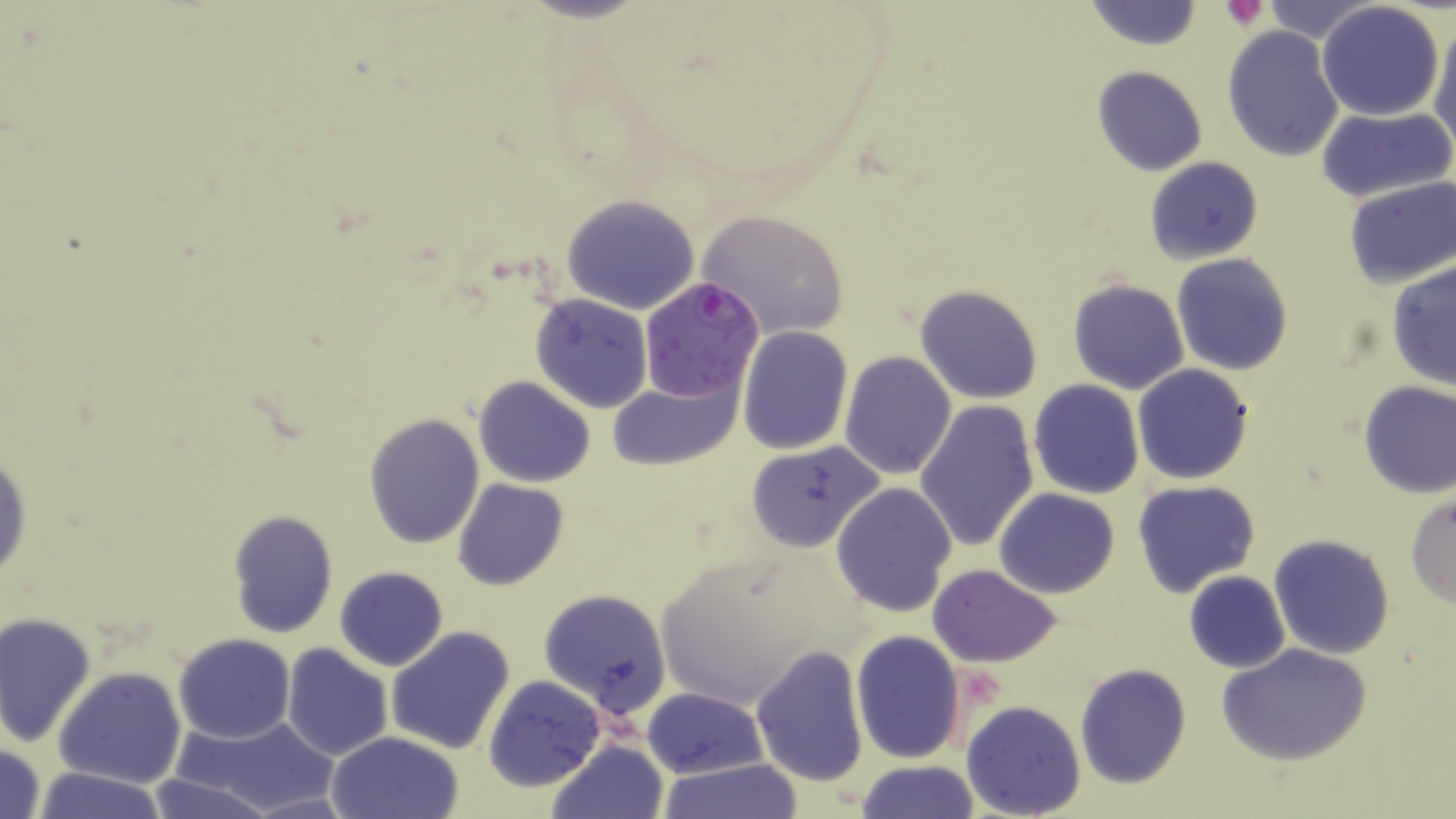
Approximate bounding boxes as (x1,y1)-(x2,y2) corner pairs in pixels. Plasmodium falciparum-infected red blood cell locations: (637,277)-(763,403). Platelet locations: (1222,1)-(1271,31). Uninfected red blood cell locations: (1085,0)-(1202,52), (1256,0)-(1383,45), (1315,2)-(1445,122), (1430,12)-(1456,149), (1222,27)-(1341,158), (1091,65)-(1207,176), (1316,105)-(1455,204), (1143,156)-(1262,265), (1343,178)-(1456,288), (561,195)-(701,314), (696,208)-(849,339), (1172,253)-(1293,374), (1387,262)-(1456,391), (1066,278)-(1190,394), (915,285)-(1042,403), (531,292)-(652,411), (737,325)-(852,453), (839,351)-(956,479), (1132,364)-(1254,484), (474,376)-(595,488), (608,376)-(741,472), (1029,378)-(1144,499), (1357,379)-(1456,497), (915,400)-(1038,551), (363,412)-(485,548), (0,441)-(32,589), (744,442)-(886,552), (451,478)-(570,591), (1131,481)-(1261,599), (832,483)-(958,616), (995,488)-(1119,598), (1406,494)-(1456,606), (226,509)-(339,640), (1268,534)-(1395,659), (650,550)-(842,707), (927,564)-(1061,667), (335,565)-(447,672), (1183,571)-(1290,673), (538,588)-(671,718), (1,612)-(97,748), (385,626)-(515,755), (849,629)-(966,763), (173,634)-(294,743), (1217,642)-(1373,767), (281,643)-(394,764), (749,644)-(870,786), (1074,662)-(1191,789), (52,667)-(187,789), (482,673)-(606,793), (643,687)-(766,779), (961,700)-(1085,818), (171,713)-(343,817), (324,731)-(463,819), (547,740)-(667,819), (0,741)-(48,819), (656,759)-(804,819), (855,760)-(979,818), (27,766)-(170,819), (142,775)-(276,819). Slide-level diagnosis: Plasmodium falciparum. May-Grünwald-Giemsa-stained preparation. Optical microscopy. 1000x magnification. Image is 1456×819 pixels. Thin blood smear. Single field of view.